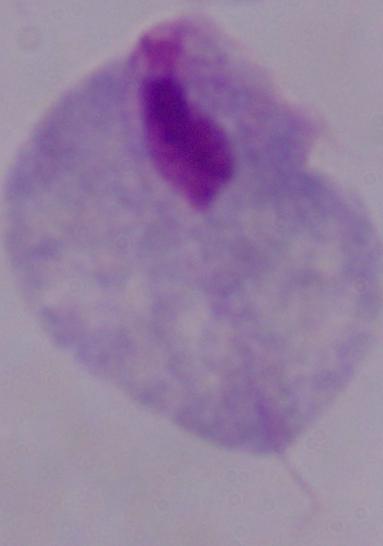

Summary:
  - Identification: trichomonad
  - Magnification: 1000x
  - Modality: photomicrograph